Assess the morphology of the erythrocytes.
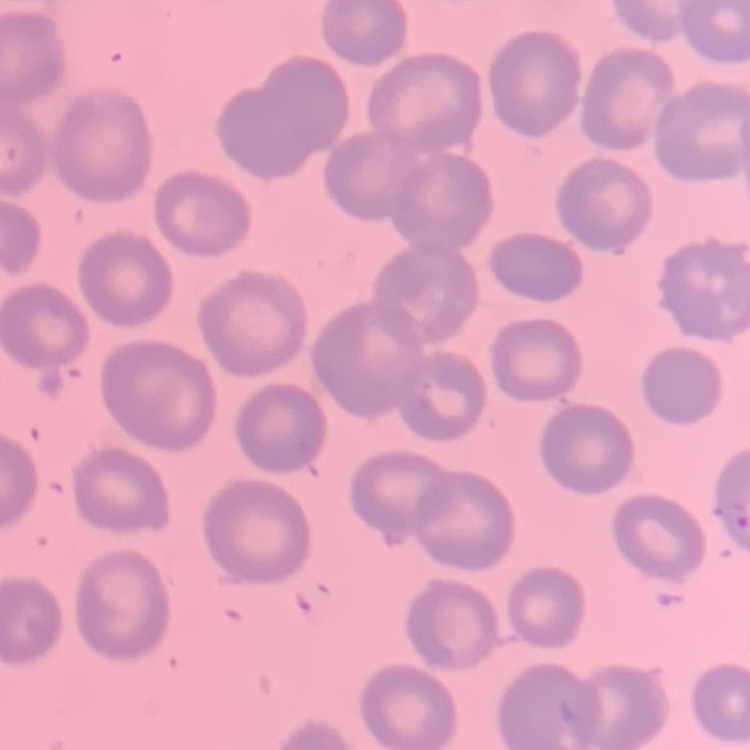

No rouleaux formation.

Thin blood film. Stained with either Field's or Giemsa. Square crop of a larger photomicrograph.